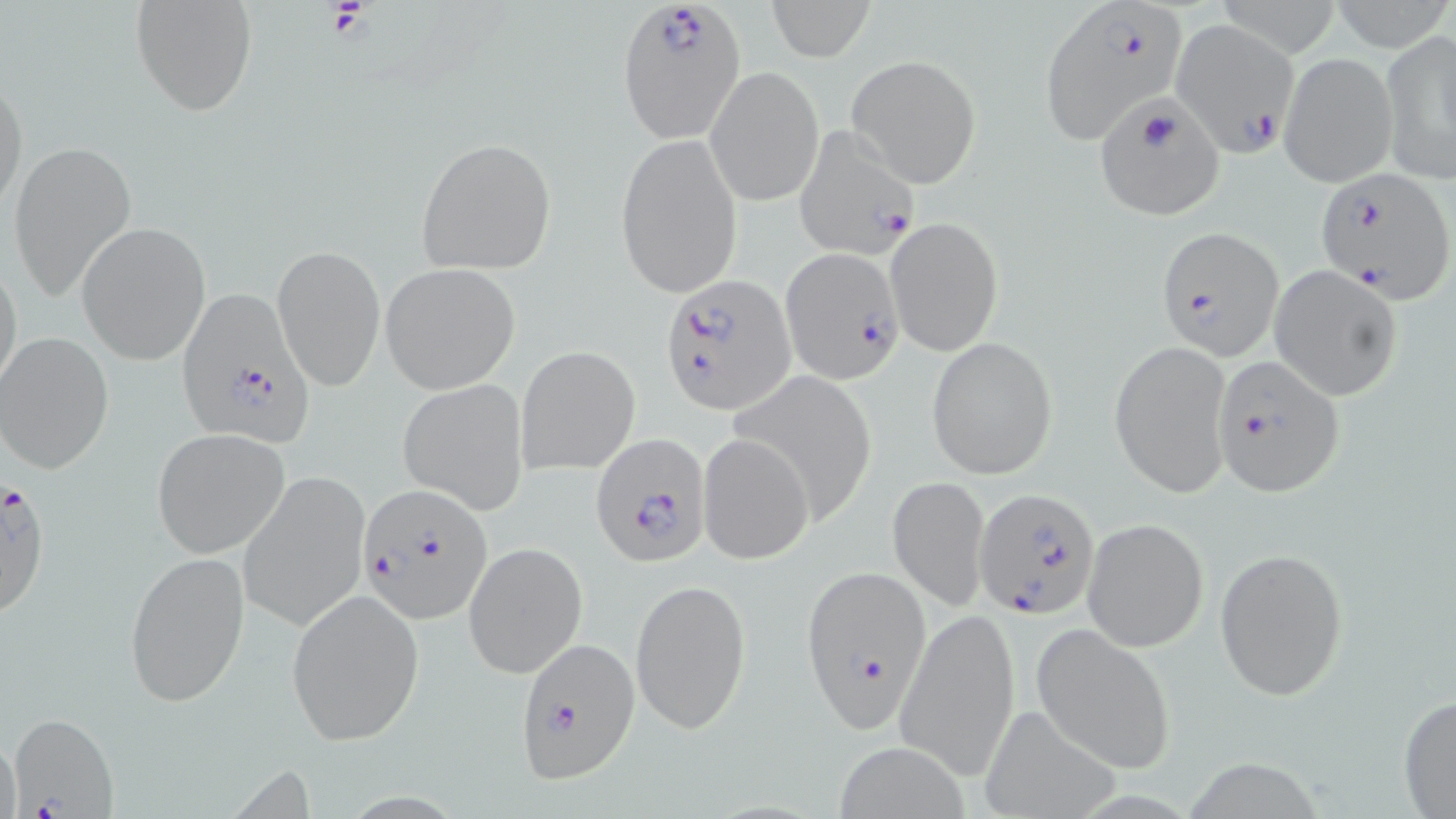

Approximate bounding boxes as named x1/y1/x2/y2 corners in pixels. Uninfected red blood cell locations: (x1=130, y1=0, x2=257, y2=118), (x1=765, y1=0, x2=872, y2=60), (x1=1379, y1=30, x2=1456, y2=186), (x1=1279, y1=52, x2=1398, y2=188), (x1=847, y1=54, x2=981, y2=188), (x1=705, y1=65, x2=825, y2=208), (x1=0, y1=69, x2=28, y2=219), (x1=615, y1=133, x2=743, y2=299), (x1=414, y1=136, x2=557, y2=274), (x1=6, y1=139, x2=138, y2=305), (x1=885, y1=215, x2=1004, y2=356), (x1=77, y1=222, x2=212, y2=364), (x1=273, y1=242, x2=385, y2=392), (x1=0, y1=251, x2=23, y2=400), (x1=380, y1=263, x2=521, y2=394), (x1=1269, y1=263, x2=1404, y2=403), (x1=2, y1=332, x2=117, y2=474), (x1=926, y1=336, x2=1058, y2=480), (x1=1109, y1=339, x2=1233, y2=499), (x1=516, y1=345, x2=641, y2=476), (x1=398, y1=379, x2=529, y2=514), (x1=151, y1=428, x2=288, y2=559), (x1=699, y1=433, x2=814, y2=562), (x1=238, y1=470, x2=370, y2=633), (x1=888, y1=474, x2=991, y2=611), (x1=1082, y1=518, x2=1210, y2=652), (x1=464, y1=543, x2=587, y2=678), (x1=1214, y1=546, x2=1349, y2=699), (x1=123, y1=550, x2=249, y2=707), (x1=630, y1=577, x2=750, y2=737), (x1=285, y1=586, x2=426, y2=747), (x1=895, y1=607, x2=1020, y2=780), (x1=1031, y1=623, x2=1177, y2=775), (x1=1397, y1=693, x2=1456, y2=818), (x1=975, y1=701, x2=1121, y2=819), (x1=833, y1=739, x2=970, y2=818). Plasmodium falciparum-infected red blood cell locations: (x1=615, y1=0, x2=745, y2=143), (x1=1039, y1=2, x2=1190, y2=138), (x1=1171, y1=18, x2=1299, y2=157), (x1=1095, y1=99, x2=1226, y2=222), (x1=794, y1=127, x2=923, y2=261), (x1=1315, y1=168, x2=1454, y2=302), (x1=1157, y1=226, x2=1284, y2=361), (x1=781, y1=249, x2=906, y2=383), (x1=661, y1=274, x2=792, y2=413), (x1=175, y1=286, x2=313, y2=447), (x1=1211, y1=356, x2=1343, y2=497), (x1=591, y1=435, x2=710, y2=566), (x1=1, y1=474, x2=53, y2=618), (x1=356, y1=484, x2=493, y2=625), (x1=975, y1=486, x2=1102, y2=620), (x1=802, y1=565, x2=931, y2=733), (x1=515, y1=638, x2=639, y2=784), (x1=6, y1=711, x2=118, y2=818). Slide-level diagnosis: Plasmodium falciparum. Image is 1456×819 pixels. Optical microscopy. May-Grünwald-Giemsa stain. Thin blood film. Captured at 1000x magnification. Single field of view.